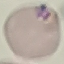

{
  "malaria_status": "parasitized",
  "preparation": "thin blood smear",
  "stain": "Giemsa",
  "image_type": "automatically extracted cell patch, resized to 64 × 64 pixels",
  "capture": "smartphone through the microscope eyepiece"
}